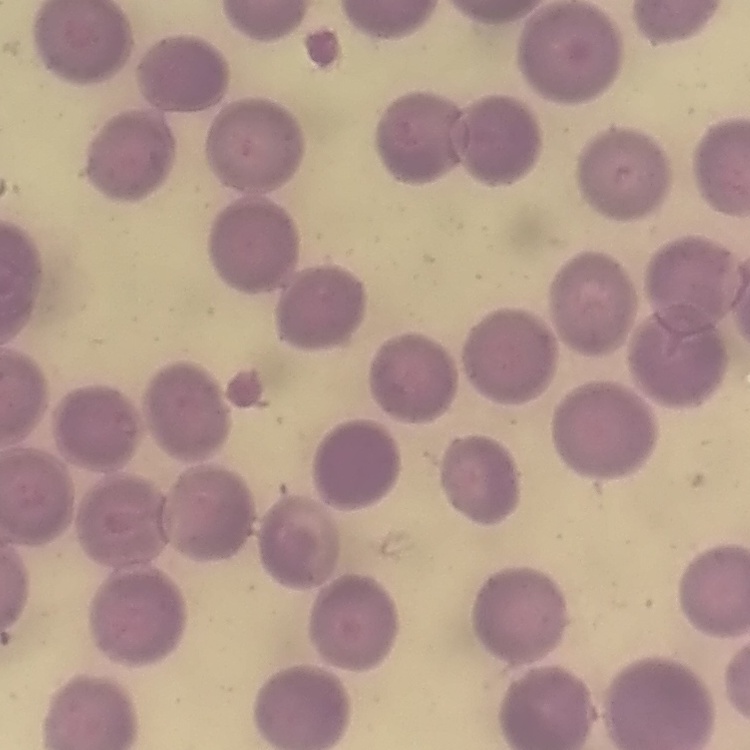

The erythrocytes exhibit no rouleaux formation. One tile cut from a larger photomicrograph. Field's or Giemsa stain. Thin blood film.